Comment on the morphology of the red blood cells.
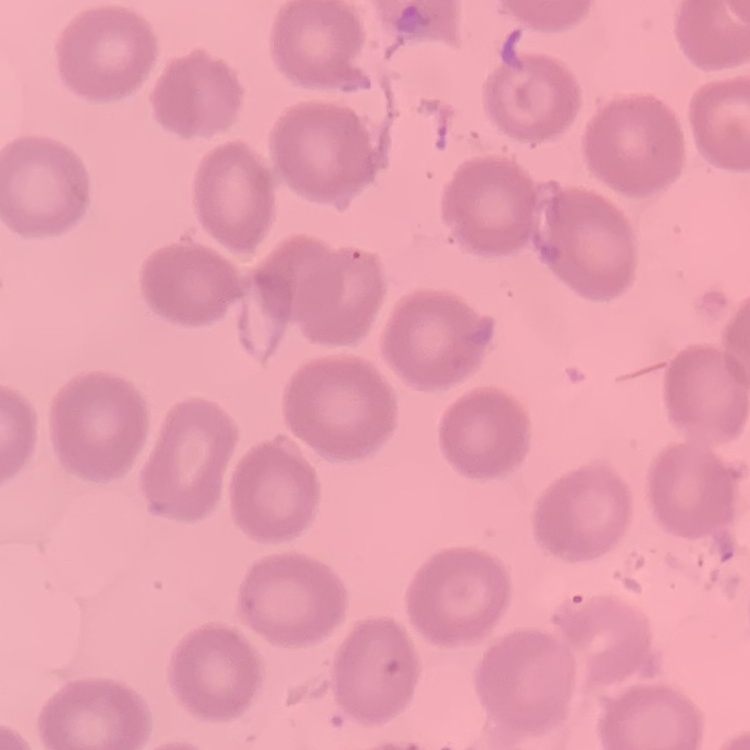
They show no rouleaux formation.

Summary:
  - Stain: Field's or Giemsa
  - Preparation: thin blood smear
  - Image type: one tile cut from a larger photomicrograph